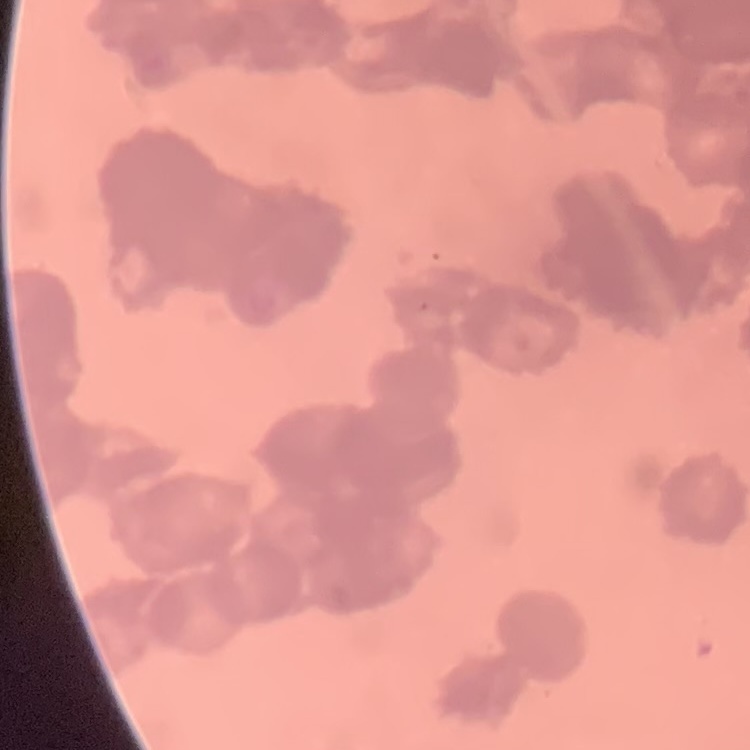

Summary:
  - Erythrocyte morphology: rouleaux formation
  - Stain: Field's or Giemsa
  - Image type: one tile cut from a larger photomicrograph
  - Preparation: thin blood film